Assess this cell for malaria.
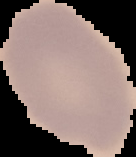

Parasitized.

image size = 136×157 pixels
image type = cell region segmented out of the field of view; surrounding area masked to black
preparation = thin blood smear